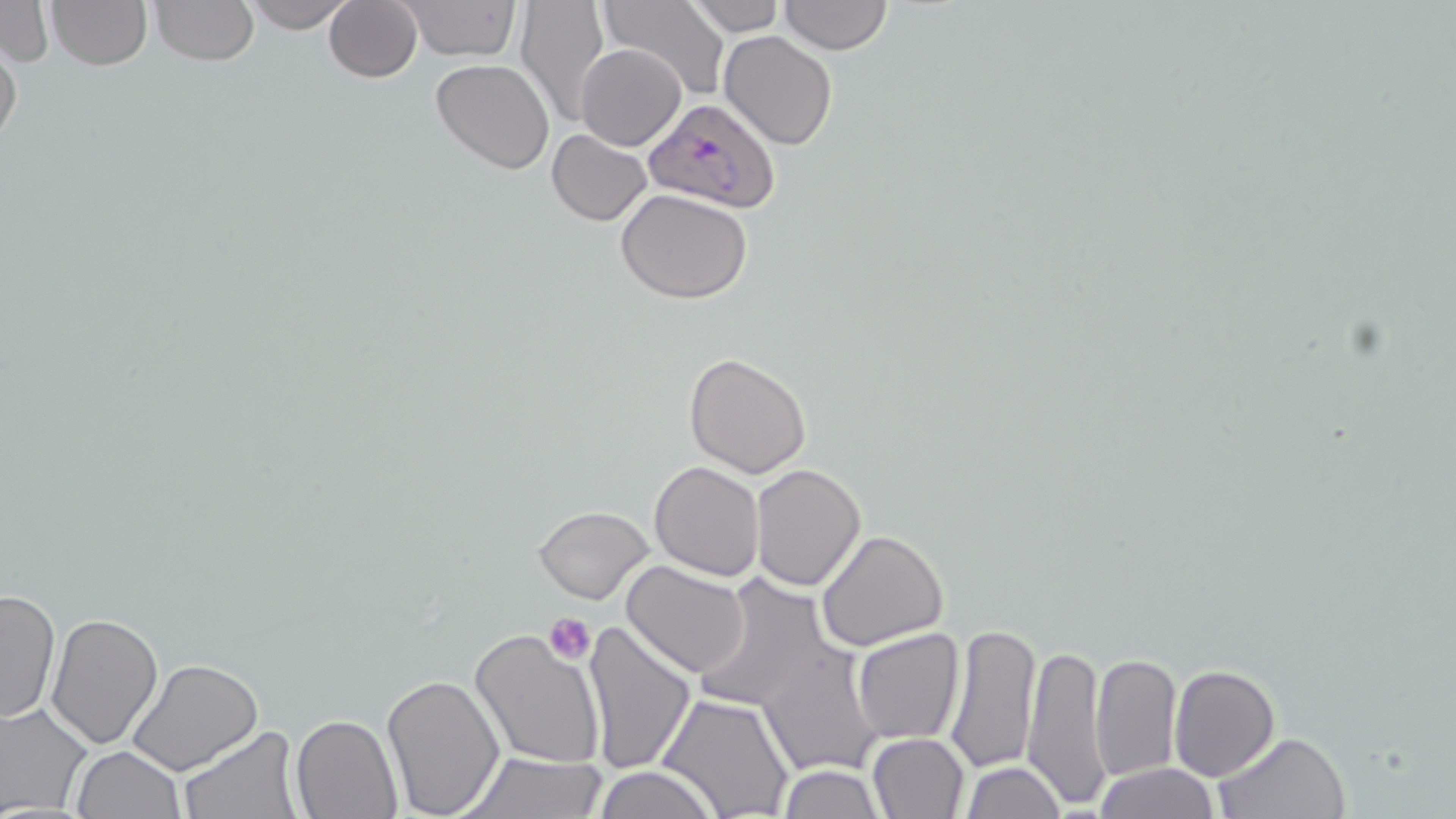

Summary:
  - Coordinate format: approximate bounding boxes as (x1, y1, x2, y2) in pixels
  - Uninfected red blood cell locations: (46, 0, 152, 71), (150, 0, 258, 65), (243, 0, 357, 33), (323, 0, 423, 84), (512, 0, 610, 128), (604, 0, 729, 101), (780, 0, 892, 54), (0, 1, 52, 68), (684, 1, 785, 35), (393, 2, 522, 62), (718, 32, 838, 149), (0, 37, 23, 156), (576, 42, 686, 151), (430, 59, 555, 174), (546, 130, 654, 225), (615, 188, 753, 304), (684, 352, 812, 478), (649, 461, 764, 581), (749, 464, 866, 591), (532, 504, 654, 604), (816, 527, 950, 650), (623, 562, 750, 678), (688, 573, 841, 719), (0, 588, 59, 725), (45, 610, 164, 748), (581, 620, 695, 775), (945, 620, 1040, 774), (466, 627, 607, 770), (851, 627, 964, 744), (1023, 641, 1110, 808), (756, 644, 884, 778), (1091, 652, 1182, 782), (129, 658, 260, 774), (1168, 665, 1279, 781), (380, 674, 505, 816), (657, 694, 795, 819), (0, 701, 94, 816), (292, 715, 403, 819), (177, 725, 301, 818), (1214, 730, 1349, 818), (866, 734, 969, 819), (72, 746, 185, 819), (459, 750, 608, 818), (960, 761, 1065, 818), (1092, 763, 1221, 818), (776, 765, 884, 818), (593, 766, 719, 819)
  - Plasmodium falciparum-infected red blood cell locations: (642, 98, 781, 216)
  - Platelet locations: (546, 615, 594, 661)
  - Slide-level diagnosis: Plasmodium falciparum
  - Preparation: thin blood film
  - Stain: May-Grünwald-Giemsa
  - Magnification: 1000x
  - Image size: 1456×819 pixels
  - Field of view: single
  - Modality: light microscopy